Assess this cell for malaria.
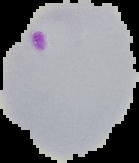
It is parasitized.

Summary:
  - Image type: segmented cell region on a black background
  - Preparation: thin blood smear
  - Image size: 139×163 pixels